Report the malaria status of this cell.
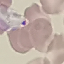
It is uninfected.

stain = Giemsa
capture = smartphone camera at the microscope eyepiece
image type = cell patch, automatically extracted from a larger field of view and resized to 64 × 64 pixels
preparation = thin blood smear